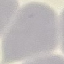
Summary:
  - Malaria status: uninfected
  - Capture: smartphone through the microscope eyepiece
  - Preparation: thin blood smear
  - Image type: cell patch, automatically extracted from a larger field of view and resized to 64 × 64 pixels
  - Stain: Giemsa